Locate every blood parasite and identify its species.
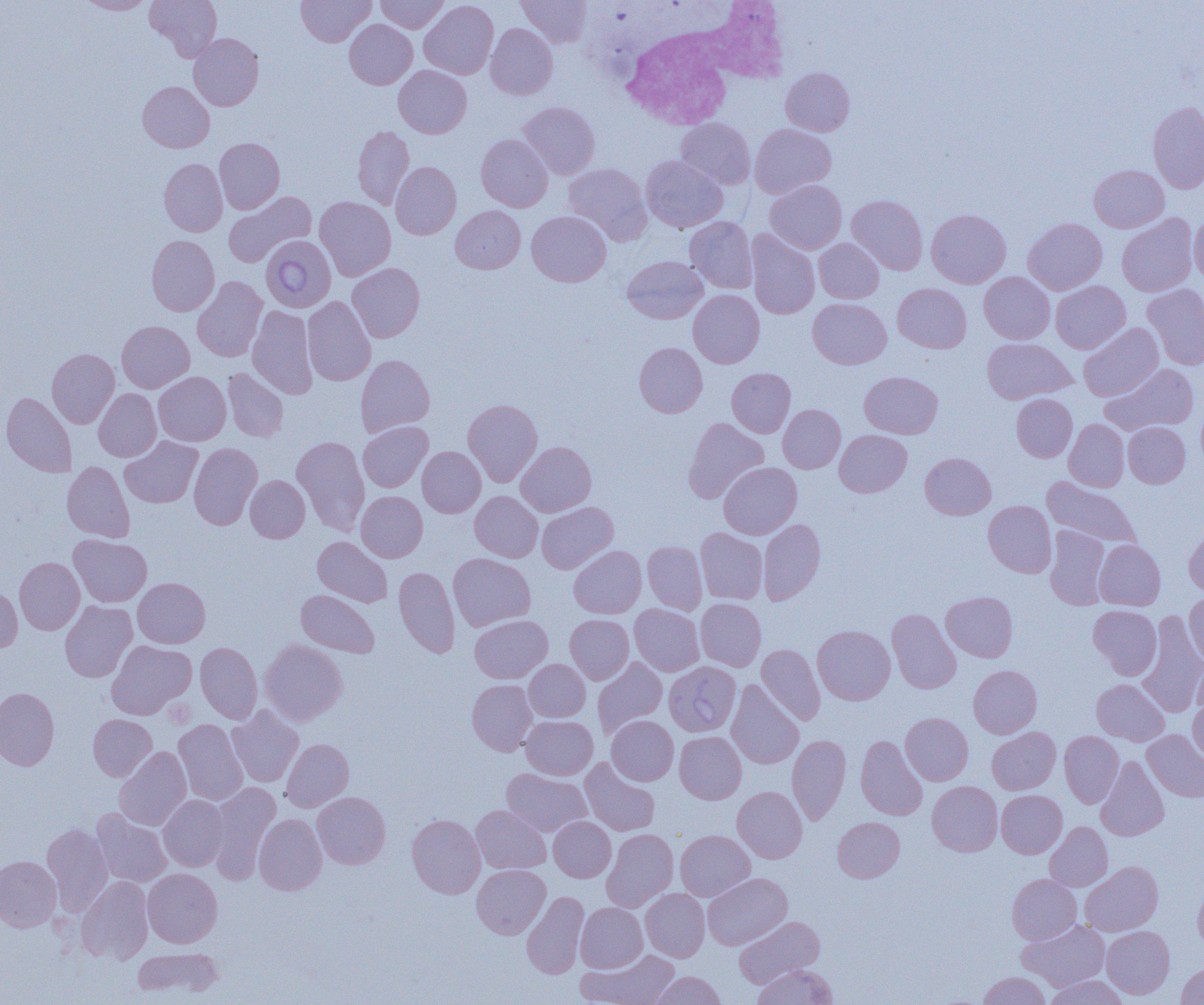
Approximate bounding boxes as (x1,y1)-(x2,y2) corner pairs in pixels.
Babesia divergens-infected red blood cells: (260,235)-(336,312), (664,662)-(741,736).
No Plasmodium falciparum, Plasmodium ovale, Plasmodium malariae, Plasmodium vivax, or Trypanosoma brucei observed.

White blood cell locations: (615,1)-(790,141). Uninfected red blood cell locations: (76,0)-(157,15), (145,0)-(223,62), (296,0)-(375,47), (376,0)-(448,33), (516,0)-(592,48), (419,1)-(499,79), (344,19)-(417,89), (485,23)-(558,100), (188,33)-(264,111), (393,65)-(471,138), (781,67)-(855,136), (137,81)-(214,153), (518,102)-(600,179), (1147,102)-(1204,193), (676,118)-(755,189), (750,124)-(836,198), (352,126)-(414,209), (476,134)-(553,211), (214,138)-(285,213), (641,155)-(728,233), (159,158)-(228,236), (391,161)-(461,240), (564,162)-(652,245), (1089,165)-(1169,233), (765,180)-(846,254), (223,191)-(317,267), (847,195)-(928,275), (315,197)-(396,280), (450,206)-(525,273), (927,209)-(1011,288), (527,211)-(611,287), (1117,213)-(1197,297), (1189,214)-(1204,285), (826,215)-(913,297), (684,216)-(758,293), (1023,218)-(1107,294), (746,230)-(820,319), (147,235)-(220,316), (814,238)-(884,303), (622,256)-(708,324), (347,263)-(425,342), (979,272)-(1055,343), (192,276)-(267,362), (1051,281)-(1130,353), (893,283)-(971,353), (1142,284)-(1204,370), (688,290)-(765,368), (302,296)-(376,386), (808,298)-(891,369), (247,305)-(318,399), (117,321)-(194,392), (1078,323)-(1163,401), (982,338)-(1076,404), (634,343)-(707,417), (47,349)-(119,428), (356,355)-(435,436), (1102,363)-(1199,435), (223,368)-(289,442), (726,368)-(796,437), (859,371)-(943,438), (153,372)-(231,446), (94,388)-(161,461), (1,392)-(76,477), (1011,394)-(1077,462), (463,399)-(543,486), (778,404)-(846,473), (683,417)-(769,503), (1064,419)-(1129,492), (358,421)-(433,492), (1123,422)-(1190,488), (835,430)-(912,497), (120,436)-(203,508), (292,436)-(370,535), (516,441)-(596,516), (188,443)-(262,530), (417,446)-(486,517), (920,452)-(995,519), (62,461)-(135,543), (719,462)-(802,539), (245,475)-(310,542), (1042,477)-(1141,549), (356,491)-(427,562), (470,491)-(542,562), (984,500)-(1056,577), (536,502)-(618,574), (758,519)-(826,605), (1184,524)-(1204,597), (1044,526)-(1110,610), (695,528)-(768,604), (69,535)-(152,607), (312,536)-(392,607), (1094,540)-(1165,610), (642,541)-(707,614), (569,545)-(646,618), (448,553)-(535,631), (14,557)-(84,635), (393,566)-(460,657), (133,577)-(210,648), (0,584)-(22,653), (296,589)-(379,658), (941,591)-(1018,662), (1184,592)-(1204,665), (695,598)-(766,671), (60,601)-(137,682), (629,604)-(704,676), (1088,605)-(1162,679), (887,609)-(962,694), (1138,612)-(1204,716), (565,614)-(633,684), (469,615)-(552,683), (812,625)-(895,705), (259,639)-(347,726), (106,640)-(196,719), (196,642)-(262,724), (757,644)-(825,724), (1192,654)-(1204,721), (593,657)-(667,738), (524,659)-(590,722), (968,665)-(1042,738), (467,679)-(538,755), (1091,679)-(1169,745), (726,680)-(804,769), (0,687)-(59,770), (1187,695)-(1204,764), (226,706)-(304,787), (900,712)-(973,785), (88,714)-(157,781), (521,716)-(597,779), (607,716)-(678,785), (173,720)-(248,805), (987,727)-(1060,794), (1142,730)-(1204,802), (675,731)-(746,804), (1060,731)-(1123,807), (787,734)-(851,825), (856,735)-(927,820), (280,738)-(354,812), (114,747)-(192,830), (1096,757)-(1169,841), (580,758)-(660,836), (502,768)-(591,837), (208,780)-(281,880), (927,781)-(1002,856), (732,786)-(807,863), (996,790)-(1067,858), (312,792)-(391,869), (158,795)-(229,871), (471,805)-(551,874), (92,808)-(171,887), (254,814)-(327,895), (407,814)-(485,898), (549,816)-(616,882), (833,816)-(904,883), (1045,822)-(1113,891), (41,824)-(112,913), (601,829)-(678,911), (675,830)-(755,900), (0,855)-(62,932), (1080,861)-(1163,936), (472,864)-(550,939), (142,868)-(222,948), (703,873)-(792,950), (1007,874)-(1081,944), (76,876)-(154,964), (1193,880)-(1204,951), (641,889)-(710,962), (521,891)-(589,978), (576,902)-(647,972), (734,915)-(825,988), (1018,920)-(1110,990), (1101,926)-(1174,999), (132,947)-(223,998), (578,949)-(679,1005), (1176,962)-(1204,1004), (753,964)-(837,1005), (648,971)-(727,1005), (979,972)-(1049,1005), (1044,975)-(1129,1005). Slide-level diagnosis: Babesia divergens. Single field of view. 1000x magnification. Image is 1204×1005 pixels. Optical microscopy. Thin blood smear.